State which parasite is depicted.
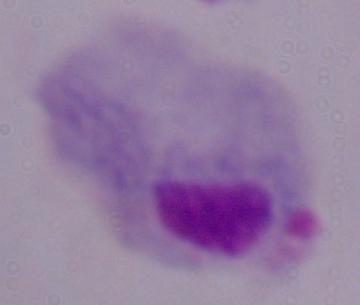

This is a trichomonad.

Summary:
  - Magnification: 1000x
  - Modality: photomicrograph